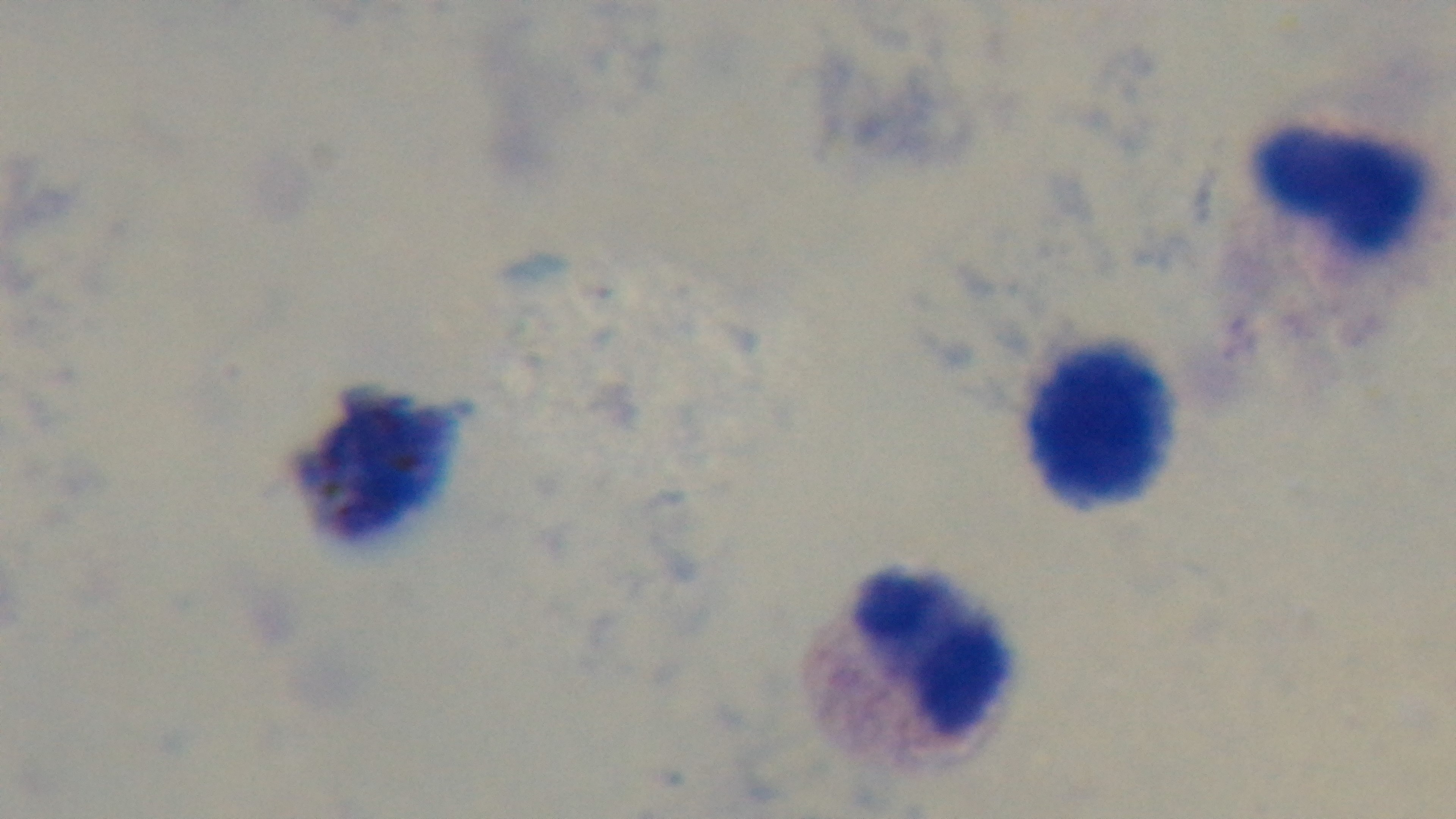
Summary:
  - Preparation: thick smear
  - Modality: light microscopy
  - Field of view: one from the slide
  - Malaria status: negative
  - Objective: 100x oil immersion
  - Stain: Giemsa
  - Capture: mounted 4K digital camera